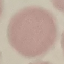

Result: no malaria parasites seen. Thin smear of blood. Automatically extracted cell patch, resized to 64 × 64 pixels. Giemsa-stained preparation. Acquired by smartphone through the microscope eyepiece.